Identify the parasite.
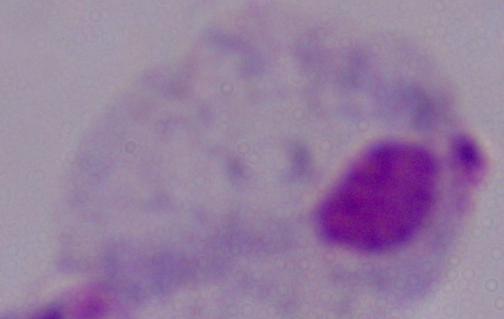

This is a trichomonad.

Captured at 1000x magnification. Photomicrograph.